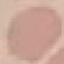 Result: no malaria parasites detected. Photographed with a smartphone camera at the microscope eyepiece. Thin blood smear. Giemsa-stained preparation. Automatically extracted cell patch, resized to 64 × 64 pixels.